Report the malaria status of this cell.
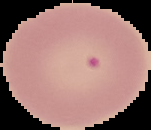
Uninfected.

image type = segmented cell region on a black background
image size = 151×130 pixels
preparation = thin blood film